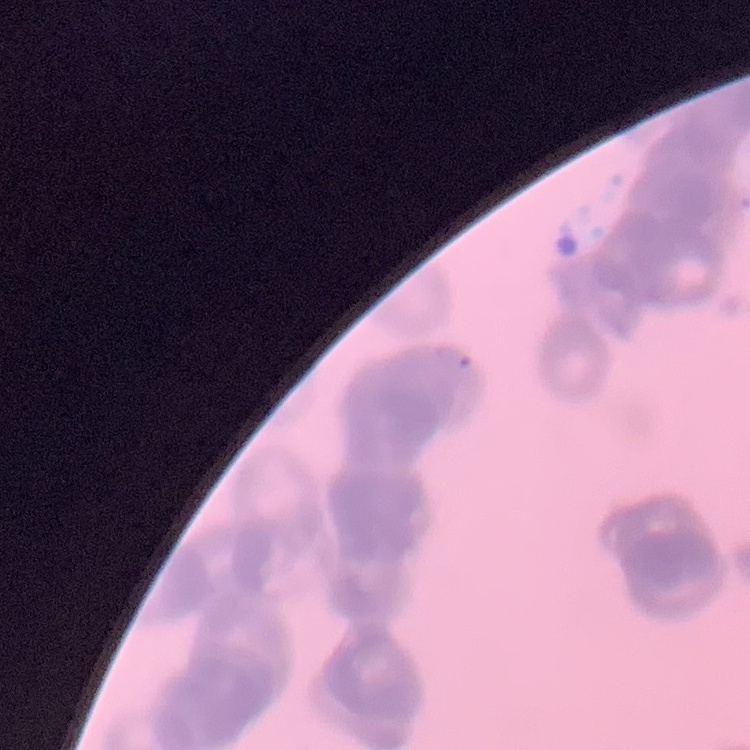

The erythrocytes exhibit rouleaux formation. Square crop of a larger photomicrograph. Thin blood film. Field's or Giemsa stain.